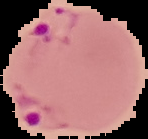

Result: malaria parasites identified. From a thin blood smear. Image is 148×139 pixels. Cell region segmented out of the field of view; the surrounding area is masked to black.